Assess this cell for malaria.
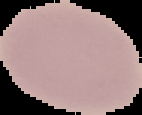
It is uninfected.

From a thin blood smear. Image is 142×115 pixels. The area outside the segmented cell region is set to black.